State which parasite is depicted.
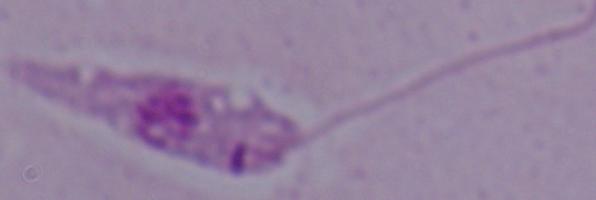

Leishmania.

{
  "magnification": "1000x",
  "modality": "micrograph"
}